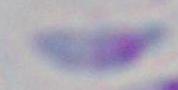

Summary:
  - Identification: Toxoplasma gondii
  - Magnification: 1000x
  - Modality: micrograph